Describe the morphology of the red blood cells.
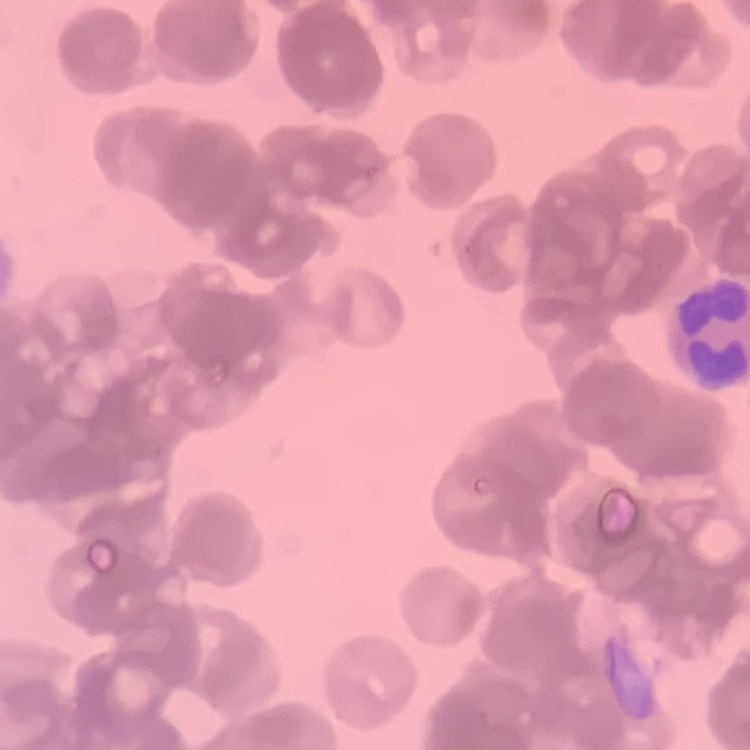
They show rouleaux formation.

preparation: thin peripheral smear
image_type: one tile cut from a larger photomicrograph
stain: Field's or Giemsa